Report the malaria status of this cell.
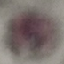
It is uninfected.

Summary:
  - Preparation: thin smear
  - Stain: Giemsa
  - Image type: automatically extracted cell patch, resized to 64 × 64 pixels
  - Capture: smartphone camera at the microscope eyepiece